Assess this cell for malaria.
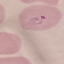
Parasitized.

Acquired by smartphone through the microscope eyepiece. Cell patch, automatically extracted from a larger field of view and resized to 64 × 64 pixels. Thin blood smear. Giemsa stain.